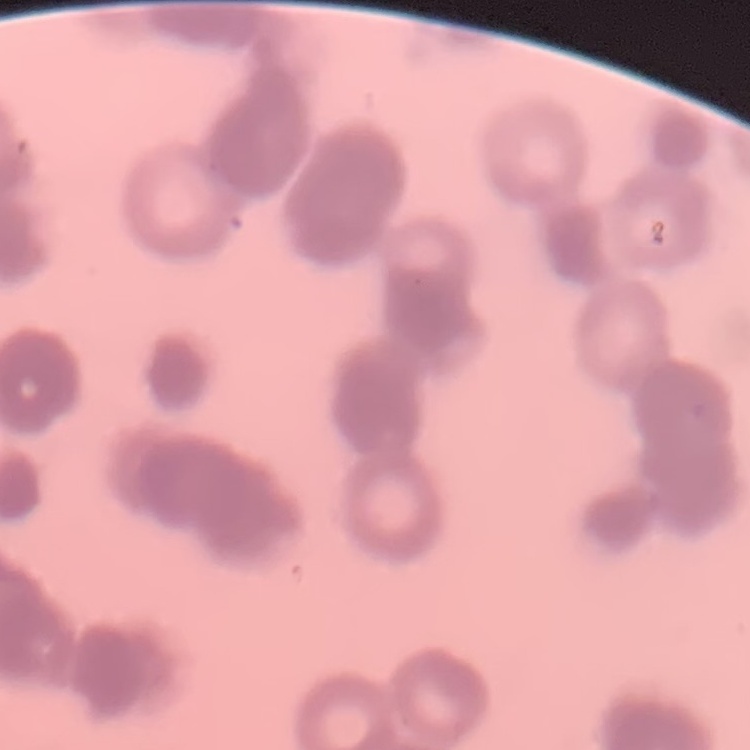 The red blood cells show rouleaux formation. Thin peripheral smear. Stained with either Field's or Giemsa. One tile cut from a larger photomicrograph.